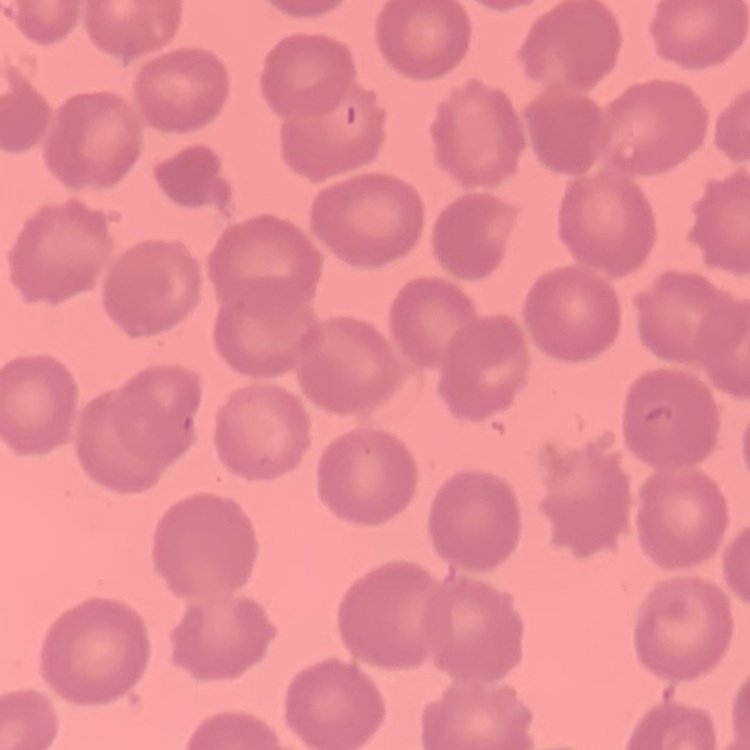

red blood cell morphology = no rouleaux formation
stain = Field's or Giemsa
preparation = thin peripheral smear
image type = one tile cut from a larger photomicrograph